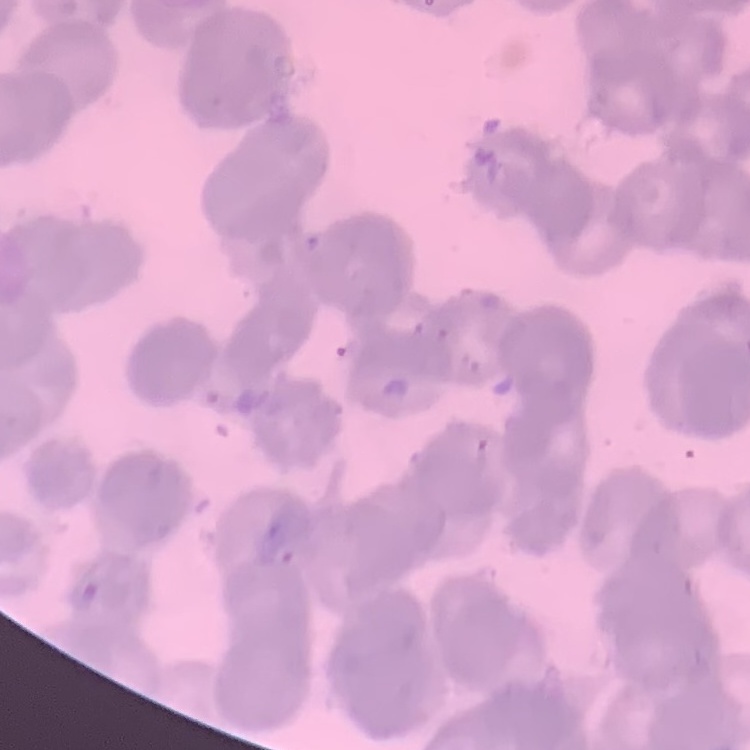
red blood cell morphology = rouleaux formation
image type = square crop of a larger photomicrograph
stain = Field's or Giemsa
preparation = thin blood film